State the preparation type.
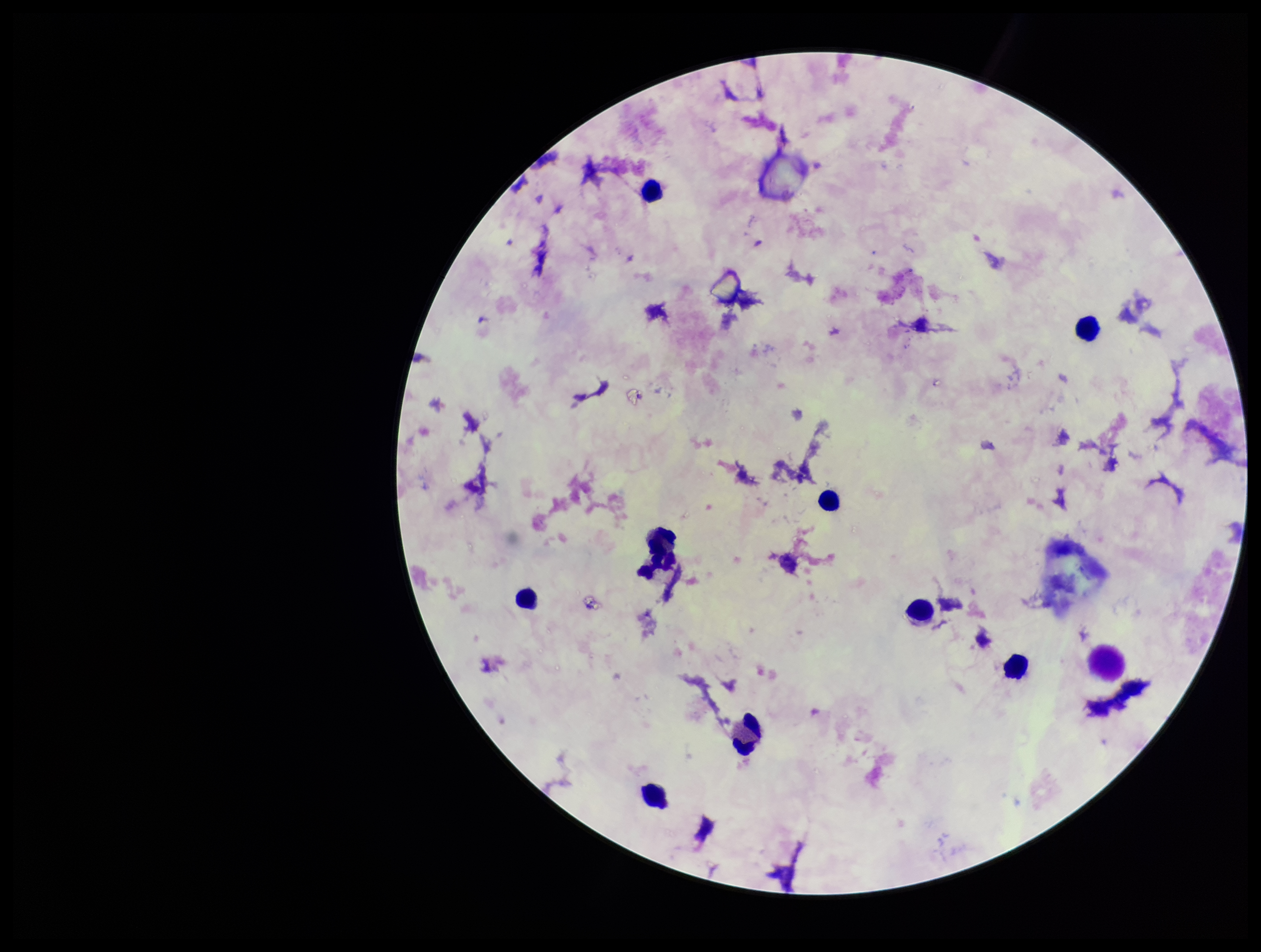
It is a thick blood smear.

One field from this slide. Stained with Giemsa. Plasmodium parasites: none detected. Patient malaria status: negative. Parasite count: 0. Leukocyte count: 9. Smartphone photograph taken through the eyepiece of a microscope. Image is 1261×952 pixels.